Report the malaria status of this cell.
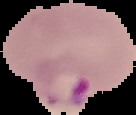

Parasitized.

image_type: cell region segmented out of the field of view; surrounding area masked to black
preparation: thin blood smear
image_size: 136×115 pixels